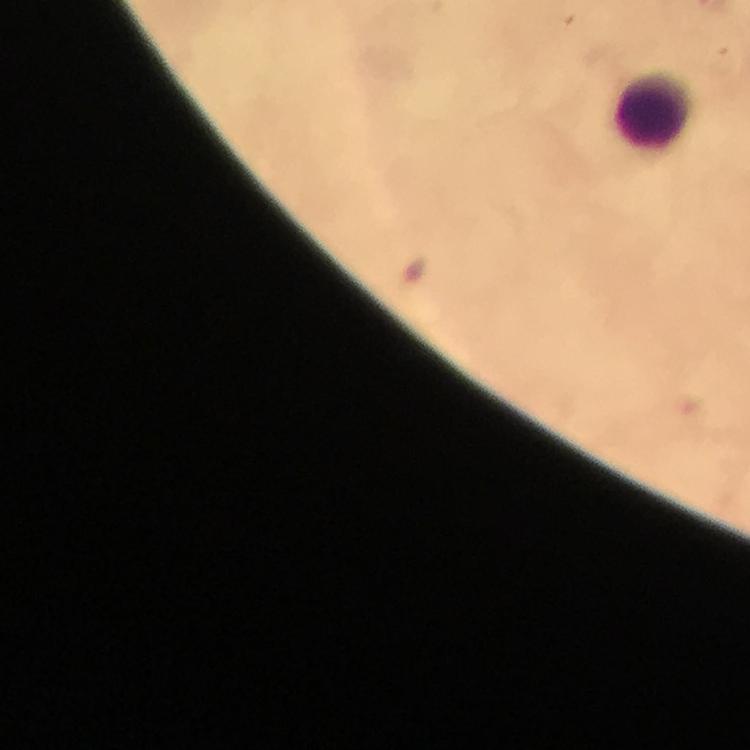
leukocyte_locations: 'approximate centers as (x, y) in pixels: (652, 112)'
immersion_oil: used
magnification: 100x
preparation: thick blood smear
cropped_from: a single field of view
malaria_parasites: none detected
image_size: 750×750 pixels
capture: smartphone photograph through a microscope
stain: Giemsa
context: from a malaria diagnostic workup